Report the malaria status of this cell.
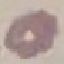

Uninfected.

image type = automatically extracted cell patch, resized to 64 × 64 pixels
stain = Giemsa
capture = smartphone through the microscope eyepiece
preparation = thin blood film